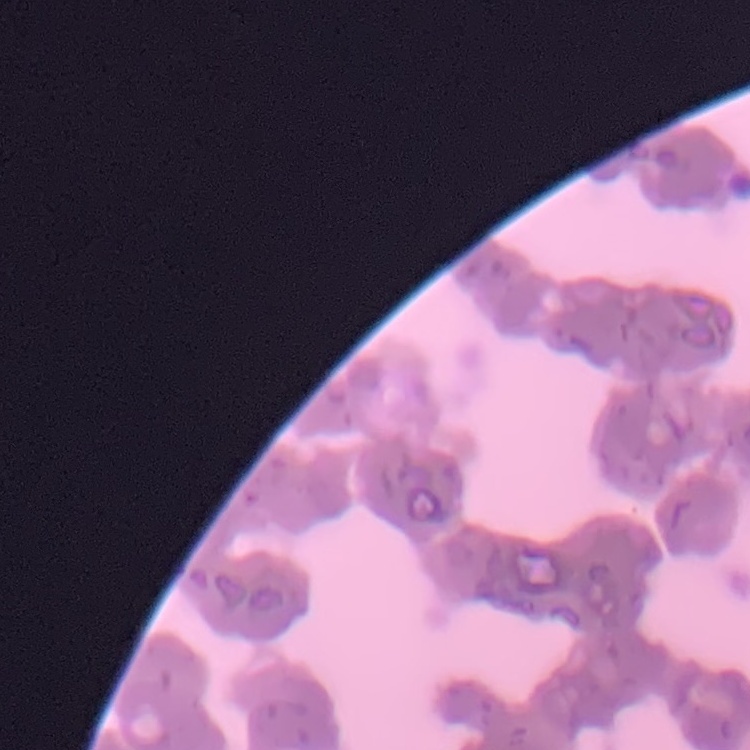

erythrocyte morphology = rouleaux formation
stain = Field's or Giemsa
image type = square crop of a larger photomicrograph
preparation = thin blood smear